State which parasite is depicted.
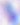
This is Toxoplasma gondii.

Captured at 400x magnification. Photomicrograph.